State which parasite is depicted.
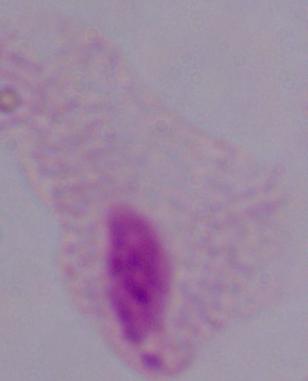

A trichomonad.

Micrograph. 1000x magnification.